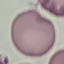 Malaria status: uninfected. Giemsa-stained preparation. Automatically extracted cell patch, resized to 64 × 64 pixels. Thin blood smear. Photographed with a smartphone camera at the microscope eyepiece.